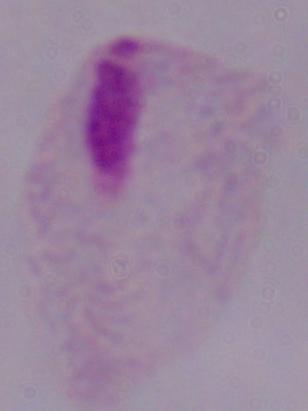
A trichomonad is seen. Photomicrograph. 1000x magnification.